Outline every artifact (platelet-like body, stain precipitate, or debris).
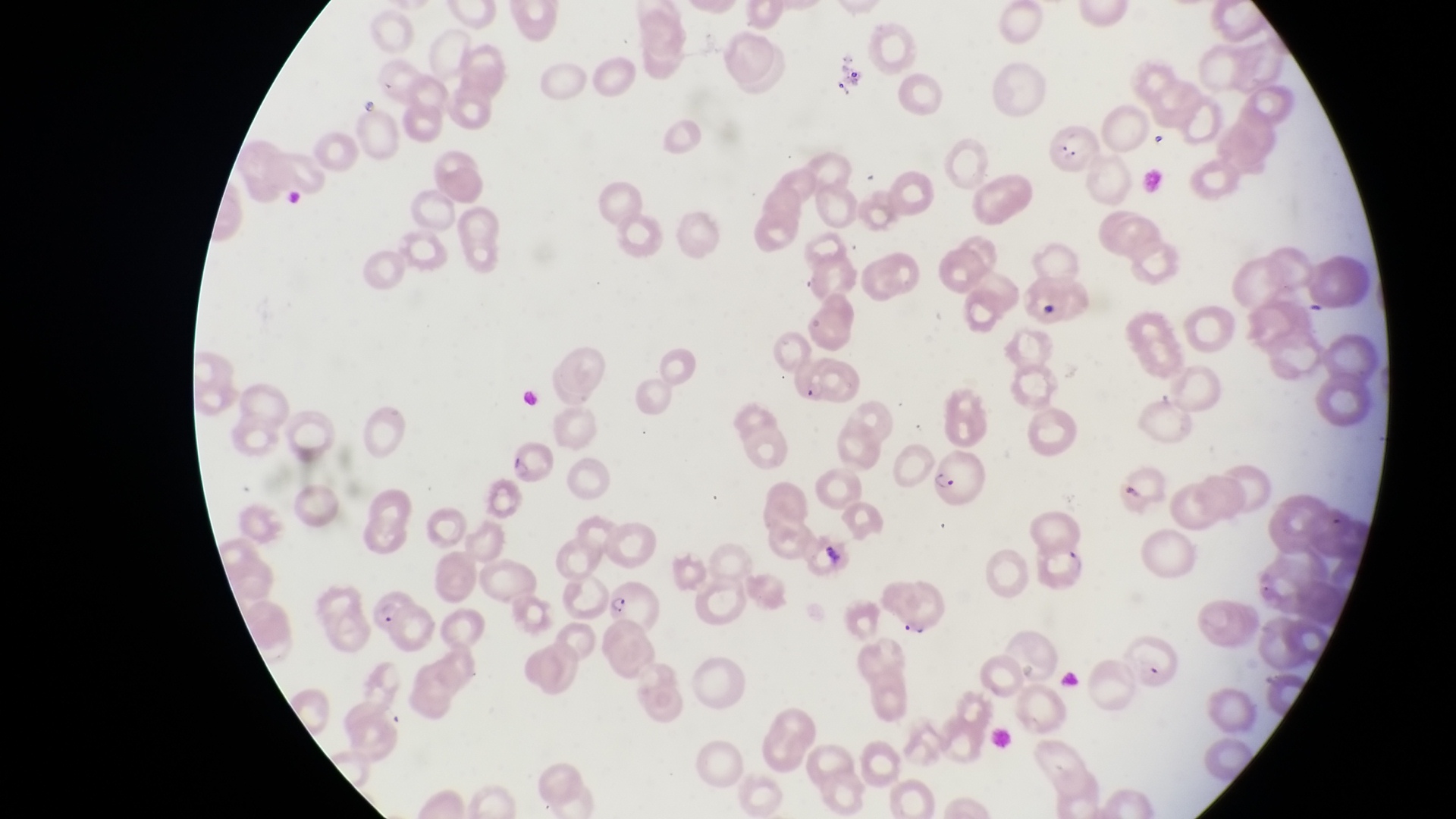

Approximate bounding boxes as {left, top, right, bottom} in pixels.
Artifacts (platelet-like body, stain precipitate, or debris): {836, 58, 869, 100}, {278, 184, 304, 207}, {1025, 293, 1057, 317}, {817, 536, 849, 570}.

{
  "image_size": "1456×819 pixels",
  "country": "Uganda",
  "capture": "smartphone photograph through the eyepiece of an Olympus CX-23 microscope",
  "preparation": "thin blood smear",
  "magnification": "1000x",
  "parasitised_red_blood_cell_locations": "approximate bounding boxes as {left, top, right, bottom} in pixels: {1052, 122, 1107, 180}, {508, 449, 553, 491}, {925, 452, 984, 505}, {1031, 536, 1087, 596}, {598, 578, 659, 634}, {360, 588, 429, 647}",
  "field_of_view": "single"
}